Report the malaria status of this cell.
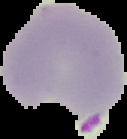

It is parasitized.

image_type: segmented cell region with the area outside set to black
image_size: 127×139 pixels
preparation: thin blood smear